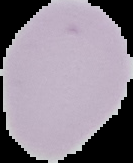
Malaria status: uninfected. Segmented cell region on a black background. From a thin blood smear. Image is 133×163 pixels.